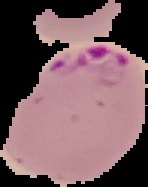
image type = cell region segmented out of the field of view; surrounding area masked to black
preparation = thin blood film
image size = 148×187 pixels
malaria status = parasitized